Locate every blood parasite and identify its species.
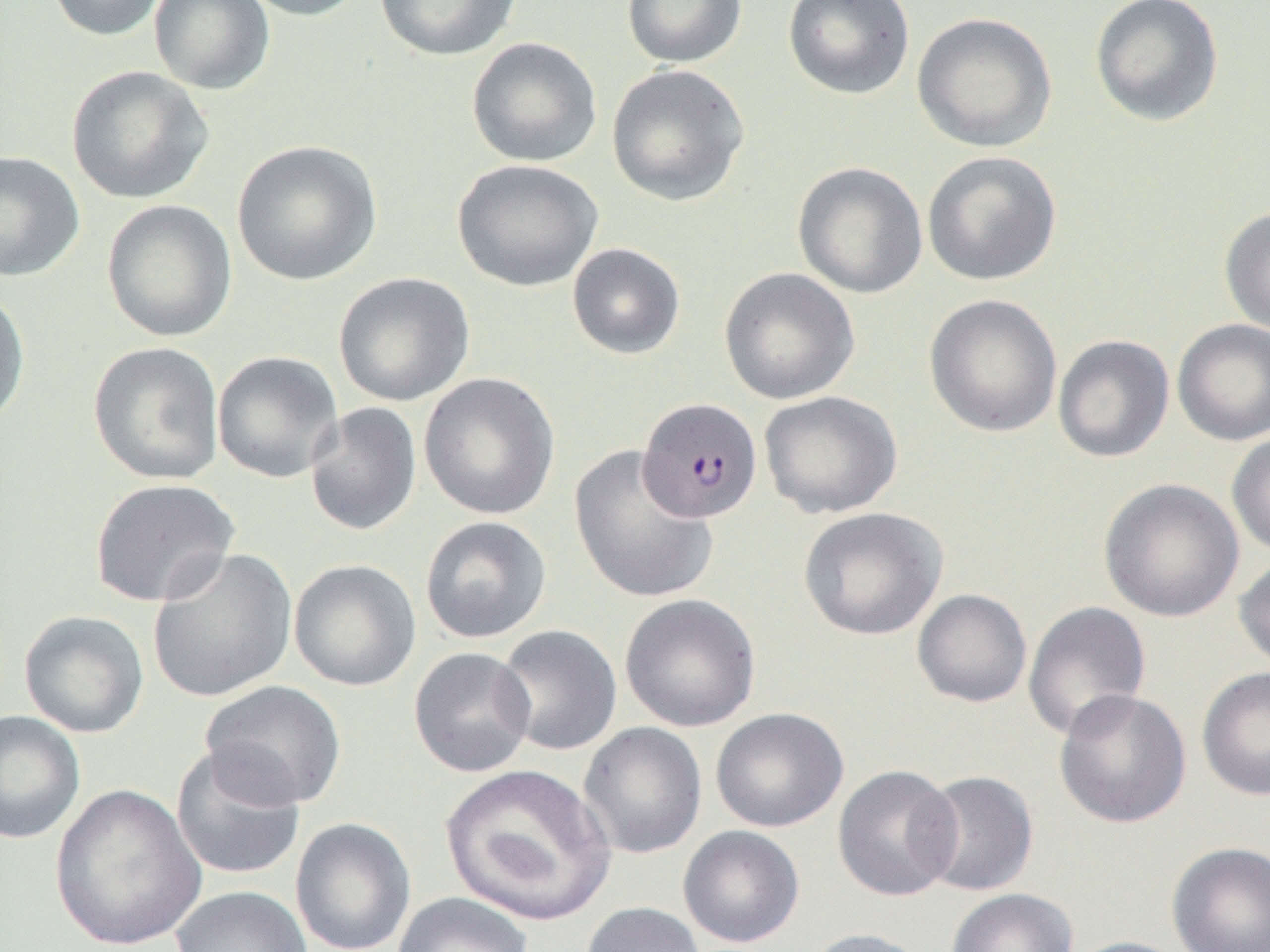

Approximate bounding boxes as [x1, y1, x2, y2] in pixels.
Plasmodium falciparum-infected red blood cells: [637, 398, 763, 523].
No Plasmodium ovale, Plasmodium malariae, Plasmodium vivax, Babesia divergens, or Trypanosoma brucei observed.

Summary:
  - Uninfected red blood cell locations: [46, 0, 171, 41], [149, 0, 275, 95], [236, 0, 371, 21], [373, 0, 522, 61], [622, 0, 748, 68], [782, 0, 915, 101], [1089, 0, 1225, 127], [911, 12, 1057, 153], [466, 37, 603, 167], [606, 64, 750, 207], [65, 65, 214, 205], [232, 140, 383, 286], [0, 150, 84, 282], [922, 150, 1062, 286], [453, 159, 603, 292], [792, 161, 928, 299], [101, 199, 238, 343], [1219, 205, 1270, 337], [567, 242, 686, 360], [719, 267, 860, 405], [333, 272, 475, 407], [0, 285, 31, 429], [923, 294, 1063, 438], [1172, 319, 1270, 446], [1052, 335, 1174, 463], [87, 341, 226, 486], [212, 350, 344, 483], [418, 372, 561, 521], [759, 390, 902, 519], [304, 402, 422, 536], [1226, 430, 1270, 558], [568, 445, 719, 604], [89, 478, 240, 607], [1099, 478, 1245, 622], [798, 507, 948, 640], [419, 515, 552, 644], [146, 547, 298, 703], [1233, 554, 1270, 673], [288, 559, 422, 691], [912, 589, 1032, 708], [619, 593, 761, 732], [1022, 600, 1152, 741], [18, 610, 150, 738], [492, 624, 622, 756], [408, 647, 537, 778], [1196, 666, 1270, 801], [200, 680, 347, 809], [1053, 688, 1192, 829], [710, 707, 849, 833], [0, 710, 86, 844], [577, 722, 708, 859], [170, 743, 307, 882], [440, 762, 616, 928], [832, 764, 962, 902], [916, 770, 1039, 897], [48, 782, 206, 952], [290, 817, 417, 952], [678, 825, 805, 948], [1166, 842, 1270, 952], [170, 885, 313, 952], [946, 888, 1078, 952], [390, 892, 534, 952], [580, 902, 707, 952], [800, 927, 932, 952], [1062, 936, 1194, 952]
  - Slide-level diagnosis: Plasmodium falciparum
  - Preparation: thin blood film
  - Field of view: one of a larger specimen
  - Modality: light microscopy
  - Magnification: 1000x
  - Image size: 1270×952 pixels